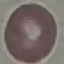

Summary:
  - Result: no malaria parasites detected
  - Image type: automatically extracted cell patch, resized to 64 × 64 pixels
  - Stain: Giemsa
  - Capture: smartphone through the microscope eyepiece
  - Preparation: thin blood smear